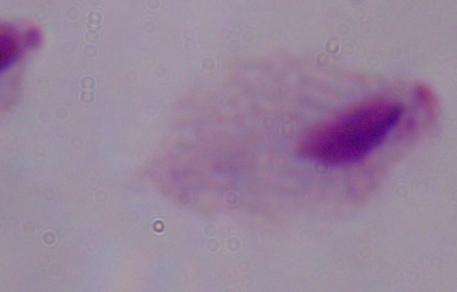
A trichomonad is shown. Photomicrograph. 1000x magnification.